Point out each Plasmodium parasite.
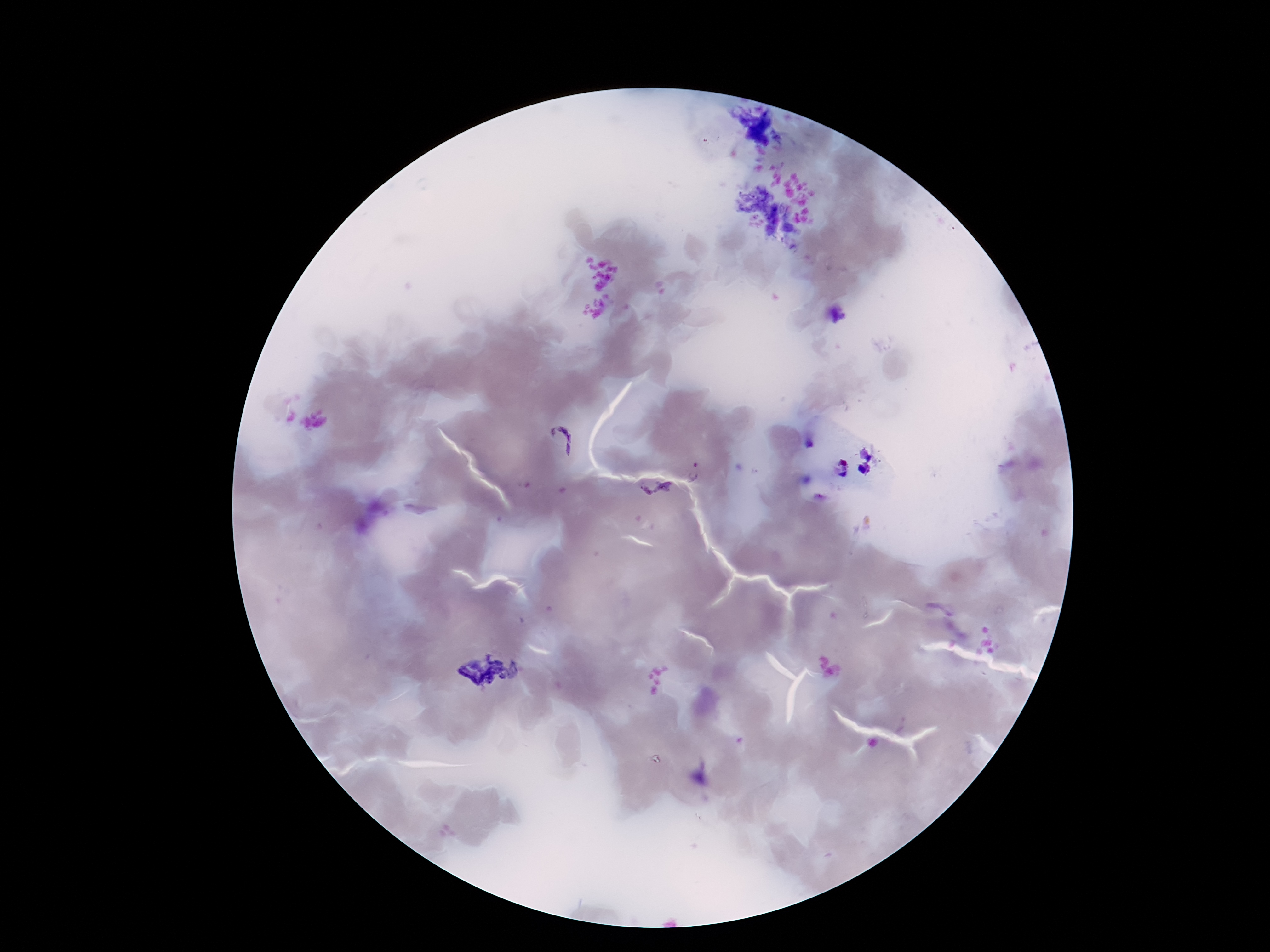
Approximate centers as {x, y} in pixels.
Plasmodium parasites: {559, 440}, {695, 472}, {656, 491}.

Summary:
  - Magnification: 100x
  - Patient malaria status: infected
  - Capture: smartphone camera through the microscope eyepiece
  - Stain: Giemsa
  - Preparation: thick peripheral-blood smear
  - Image size: 1270×952 pixels
  - Field of view: single